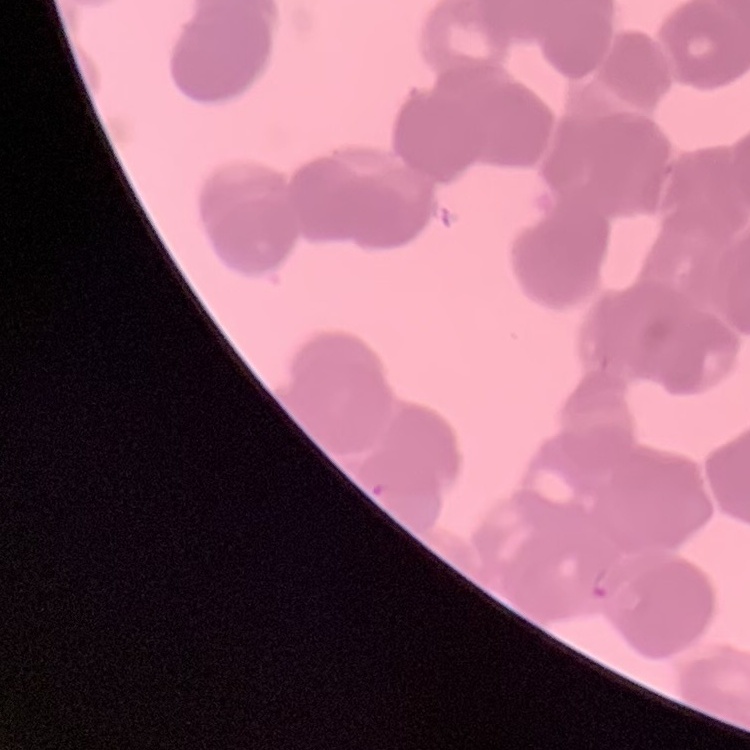
Summary:
  - Red blood cell morphology: rouleaux formation
  - Preparation: thin blood smear
  - Image type: one tile cut from a larger photomicrograph
  - Stain: Field's or Giemsa